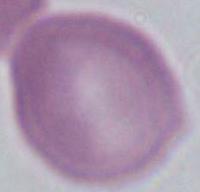

magnification = 1000x
identification = red blood cell
modality = photomicrograph